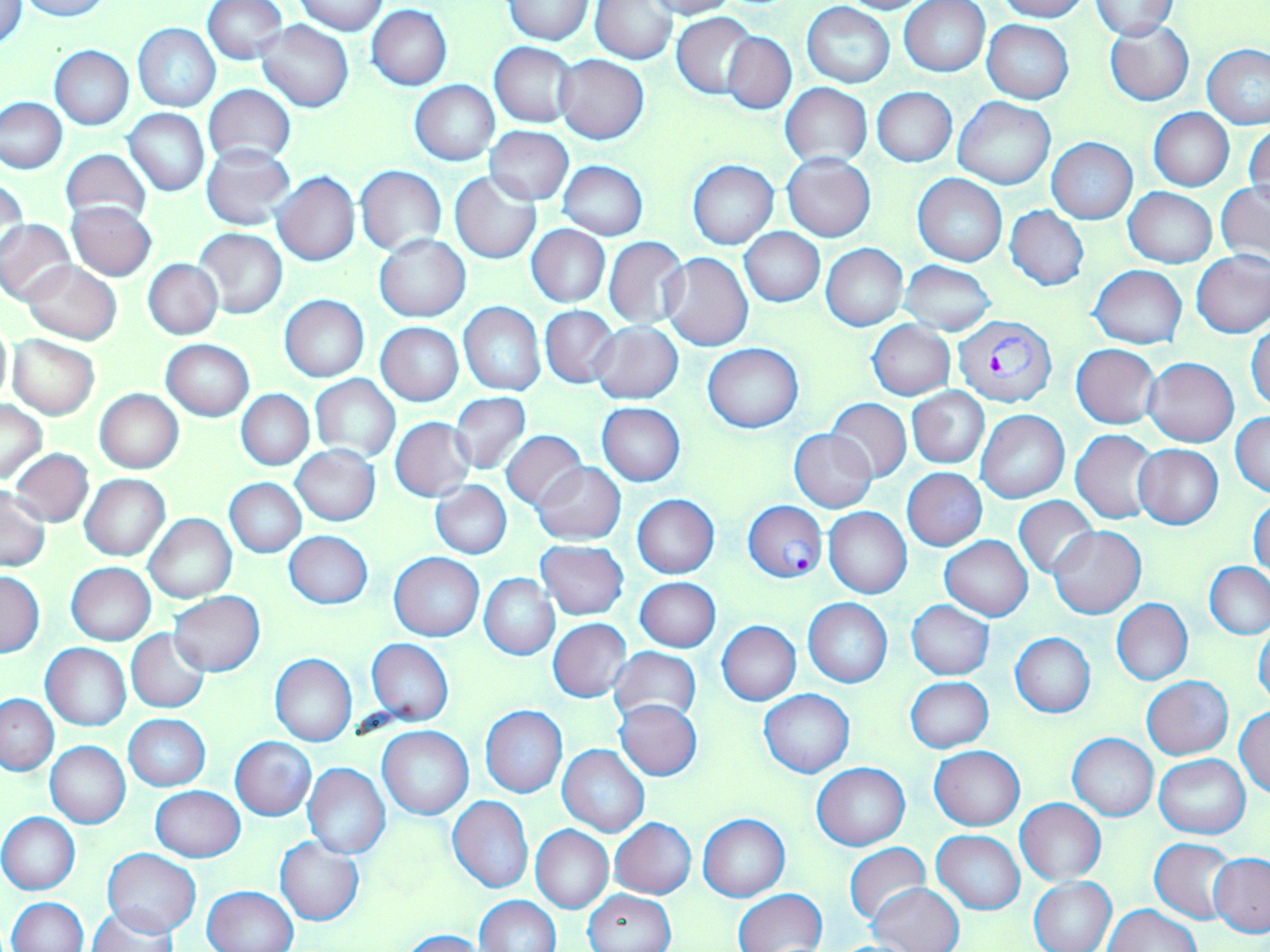
Approximate bounding boxes as [x1, y1, x2, y2] in pixels. Uninfected red blood cell locations: [1, 0, 29, 50], [15, 0, 110, 21], [201, 0, 288, 65], [295, 0, 390, 35], [641, 0, 741, 19], [831, 0, 938, 14], [992, 0, 1090, 21], [505, 1, 595, 44], [899, 1, 991, 76], [1089, 1, 1178, 39], [591, 2, 677, 62], [801, 2, 895, 87], [367, 5, 452, 90], [673, 13, 758, 99], [256, 20, 353, 113], [982, 20, 1073, 103], [1104, 20, 1195, 105], [133, 23, 221, 112], [723, 32, 796, 113], [490, 42, 578, 127], [1201, 44, 1270, 130], [49, 46, 133, 129], [555, 54, 649, 143], [410, 80, 499, 165], [782, 84, 871, 167], [203, 85, 296, 166], [872, 87, 957, 167], [1, 97, 67, 174], [953, 97, 1055, 190], [1149, 108, 1233, 191], [125, 109, 210, 196], [1245, 120, 1270, 208], [486, 125, 573, 204], [1047, 139, 1137, 223], [202, 145, 294, 230], [60, 150, 152, 227], [782, 152, 875, 241], [688, 160, 779, 249], [559, 162, 648, 239], [355, 165, 446, 253], [273, 172, 359, 266], [450, 173, 540, 264], [913, 173, 1007, 266], [1, 175, 28, 262], [1216, 182, 1270, 270], [1124, 187, 1217, 268], [67, 202, 157, 281], [1004, 206, 1089, 292], [1, 218, 76, 305], [527, 225, 609, 307], [192, 228, 287, 319], [740, 228, 825, 307], [375, 235, 469, 321], [604, 238, 688, 328], [821, 244, 907, 331], [1192, 251, 1270, 338], [661, 253, 752, 351], [143, 259, 222, 339], [21, 261, 121, 344], [900, 261, 996, 335], [1089, 266, 1187, 349], [279, 295, 368, 382], [459, 302, 545, 396], [540, 307, 618, 388], [0, 320, 13, 408], [868, 321, 955, 400], [1247, 321, 1270, 413], [375, 322, 463, 406], [591, 323, 682, 404], [8, 336, 99, 419], [162, 340, 254, 420], [702, 343, 804, 432], [1071, 344, 1161, 429], [1145, 357, 1238, 446], [310, 374, 400, 463], [908, 387, 989, 468], [94, 389, 183, 474], [237, 390, 314, 470], [449, 391, 530, 476], [826, 398, 912, 483], [0, 400, 48, 486], [597, 403, 684, 487], [976, 410, 1069, 503], [1231, 411, 1270, 497], [390, 417, 476, 501], [789, 429, 876, 512], [1071, 429, 1159, 524], [500, 430, 588, 511], [1134, 444, 1223, 529], [291, 446, 380, 525], [10, 449, 92, 527], [532, 462, 626, 545], [902, 468, 987, 551], [80, 474, 170, 561], [224, 478, 306, 558], [430, 480, 511, 559], [0, 488, 51, 571], [632, 494, 719, 577], [1014, 496, 1099, 578], [1250, 497, 1269, 579], [825, 508, 912, 599], [145, 513, 237, 603], [1049, 525, 1145, 618], [284, 531, 373, 609], [941, 536, 1032, 620], [536, 540, 629, 619], [389, 552, 484, 641], [66, 562, 156, 644], [1205, 562, 1270, 639], [1, 569, 45, 657], [479, 573, 559, 660], [635, 578, 721, 651], [169, 592, 265, 675], [803, 598, 892, 688], [1112, 598, 1193, 685], [906, 601, 994, 679], [549, 619, 632, 703], [717, 621, 800, 705], [1254, 622, 1270, 708], [125, 629, 211, 713], [1010, 632, 1095, 717], [366, 639, 453, 726], [41, 643, 131, 731], [608, 646, 700, 725], [271, 654, 356, 746], [906, 676, 992, 753], [1143, 677, 1233, 759], [760, 689, 854, 778], [0, 693, 59, 775], [615, 699, 702, 780], [1235, 705, 1270, 797], [480, 706, 567, 797], [124, 715, 209, 791], [376, 726, 472, 819], [1068, 733, 1159, 821], [230, 736, 316, 820], [46, 743, 131, 827], [558, 744, 650, 837], [930, 746, 1025, 830], [1155, 755, 1250, 838], [813, 762, 909, 849], [302, 763, 390, 859], [150, 786, 244, 861], [446, 796, 533, 893], [1016, 798, 1106, 885], [0, 812, 80, 894], [699, 814, 790, 900], [610, 818, 696, 897], [531, 825, 613, 913], [932, 830, 1025, 914], [275, 838, 365, 925], [1149, 839, 1237, 923], [844, 843, 931, 925], [104, 849, 201, 937], [844, 852, 1003, 938], [1208, 853, 1270, 938], [1029, 876, 1117, 952], [868, 882, 964, 951], [204, 885, 297, 952], [584, 889, 676, 952], [735, 889, 827, 951], [474, 895, 559, 951], [8, 896, 88, 951], [1104, 904, 1199, 952], [89, 906, 176, 951], [400, 930, 492, 952]. Plasmodium falciparum-infected red blood cell locations: [952, 314, 1056, 408], [742, 501, 828, 582]. Slide-level diagnosis: Plasmodium falciparum. Single field of view. 1000x magnification. May-Grünwald-Giemsa stain. Image is 1270×952 pixels. Thin blood smear. Optical microscopy.